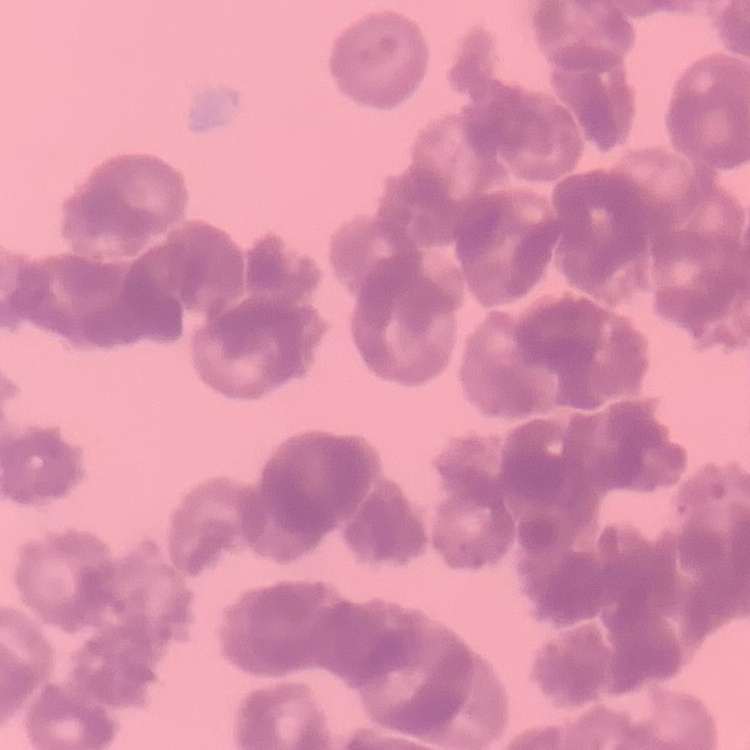
The red blood cells show rouleaux formation. Field's or Giemsa stain. Square crop of a larger photomicrograph. Thin blood film.